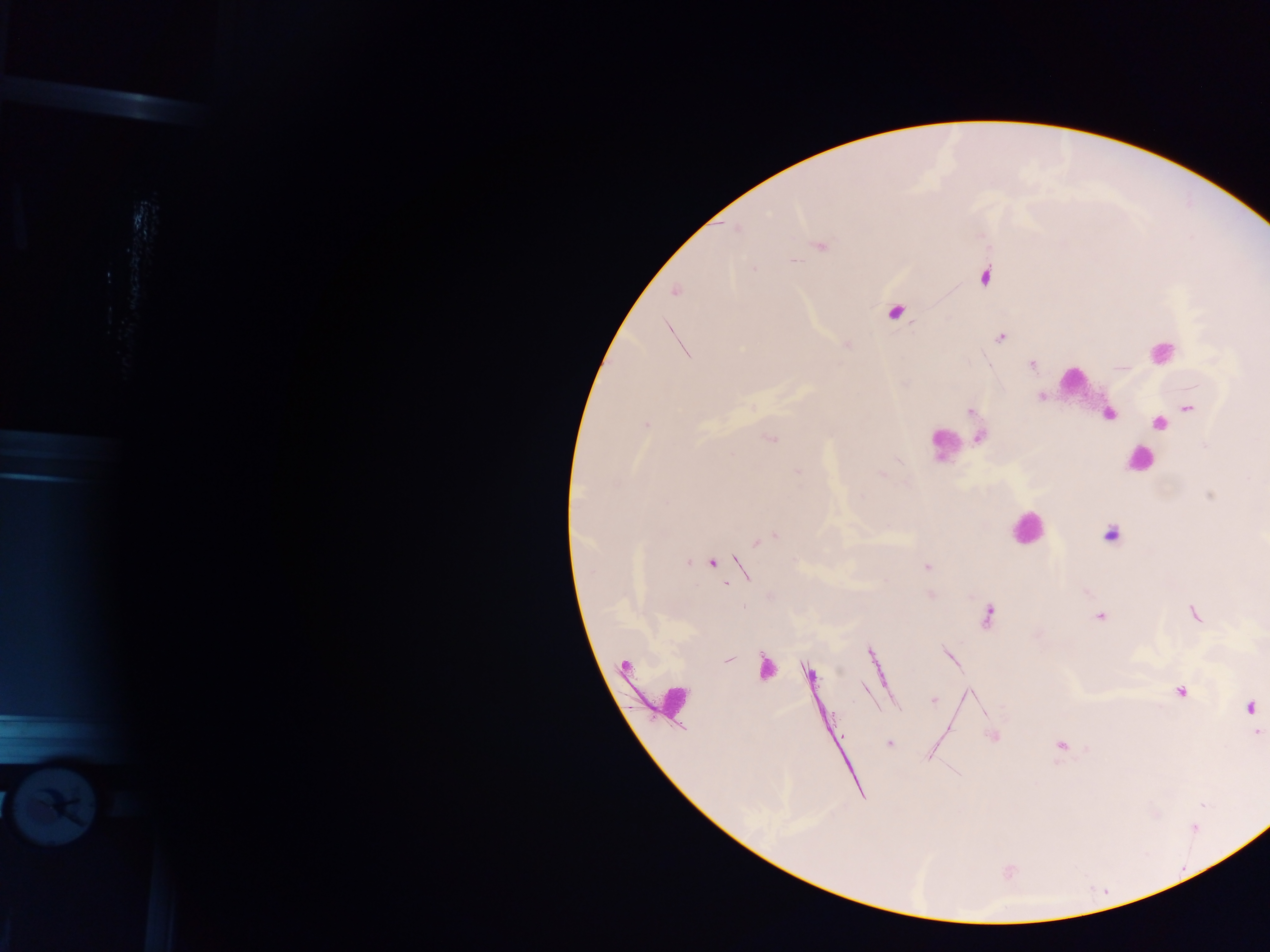

image size = 1270×952 pixels
capture = mobile-phone photograph through a microscope
field of view = single
country = Ghana
leukocyte locations = approximate centers as x y in pixels: 1160 352; 1075 380; 945 447; 1139 461; 1026 527; 674 698
preparation = thick blood film
Plasmodium parasite locations = approximate centers as x y in pixels: 822 246; 794 261; 754 268; 984 277; 675 292; 895 312; 1001 338; 1032 364; 1041 397; 1188 408; 970 411; 647 424; 1158 424; 979 438; 771 439; 1205 445; 798 471; 882 474; 1210 495; 1111 535; 770 537; 762 540; 688 563; 712 563; 923 567; 743 607; 1195 614; 987 617; 1100 617; 728 659; 766 667; 809 673; 1181 692; 934 699; 1250 706; 1258 732; 994 737; 888 744; 1061 745
object labeled both Plasmodium parasite and leukocyte by the source = approximate centers as x y in pixels: 1108 414